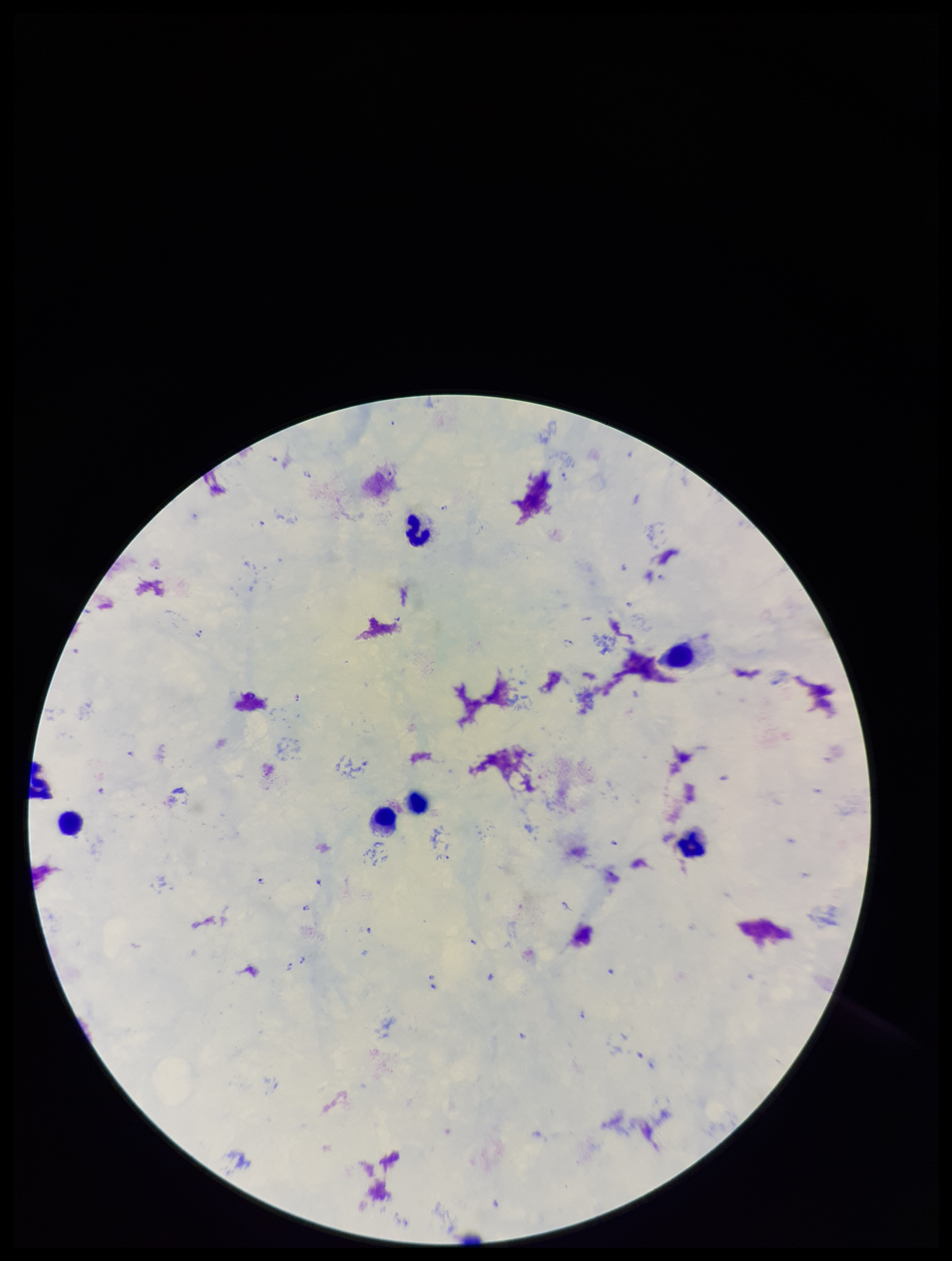

Stained with Giemsa. Image is 952×1261 pixels. Species reported for this patient: Plasmodium falciparum. Parasite count: 18. Single field of view. Patient malaria status: positive. Preparation: thick smear. Leukocyte count: 6. Plasmodium parasites: detected. Smartphone photograph taken through the eyepiece of a microscope.